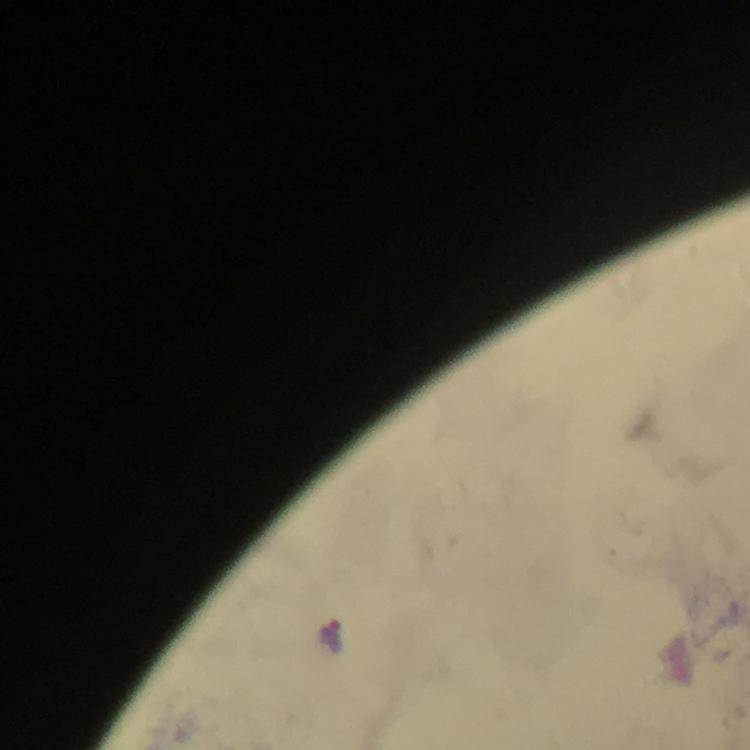
Approximate centers as (x, y) in pixels. Malaria parasite locations: (332, 635). A crop from one field of view. Immersion oil was used. From a diagnostic examination for malaria. Giemsa stain. Image is 750×750 pixels. 100x magnification. Thick blood film. Smartphone photograph taken through a microscope.